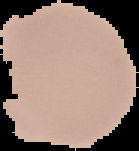

Summary:
  - Malaria status: uninfected
  - Preparation: thin blood film
  - Image type: segmented cell region on a black background
  - Image size: 139×151 pixels